Identify the parasite.
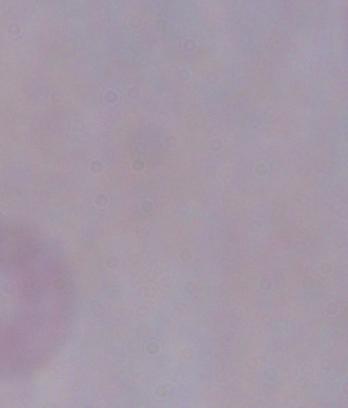

This is a trypanosome.

Photomicrograph. Captured at 1000x magnification.